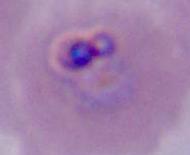

Summary:
  - Identification: Plasmodium
  - Magnification: 400x or 1000x
  - Modality: micrograph